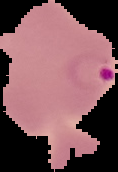

Summary:
  - Result: Plasmodium parasites identified
  - Preparation: thin blood film
  - Image type: segmented cell region on a black background
  - Image size: 118×172 pixels